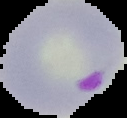
Summary:
  - Result: Plasmodium parasites identified
  - Image size: 127×118 pixels
  - Preparation: thin blood smear
  - Image type: cell region segmented out of the field of view; surrounding area masked to black